Point out every malaria parasite.
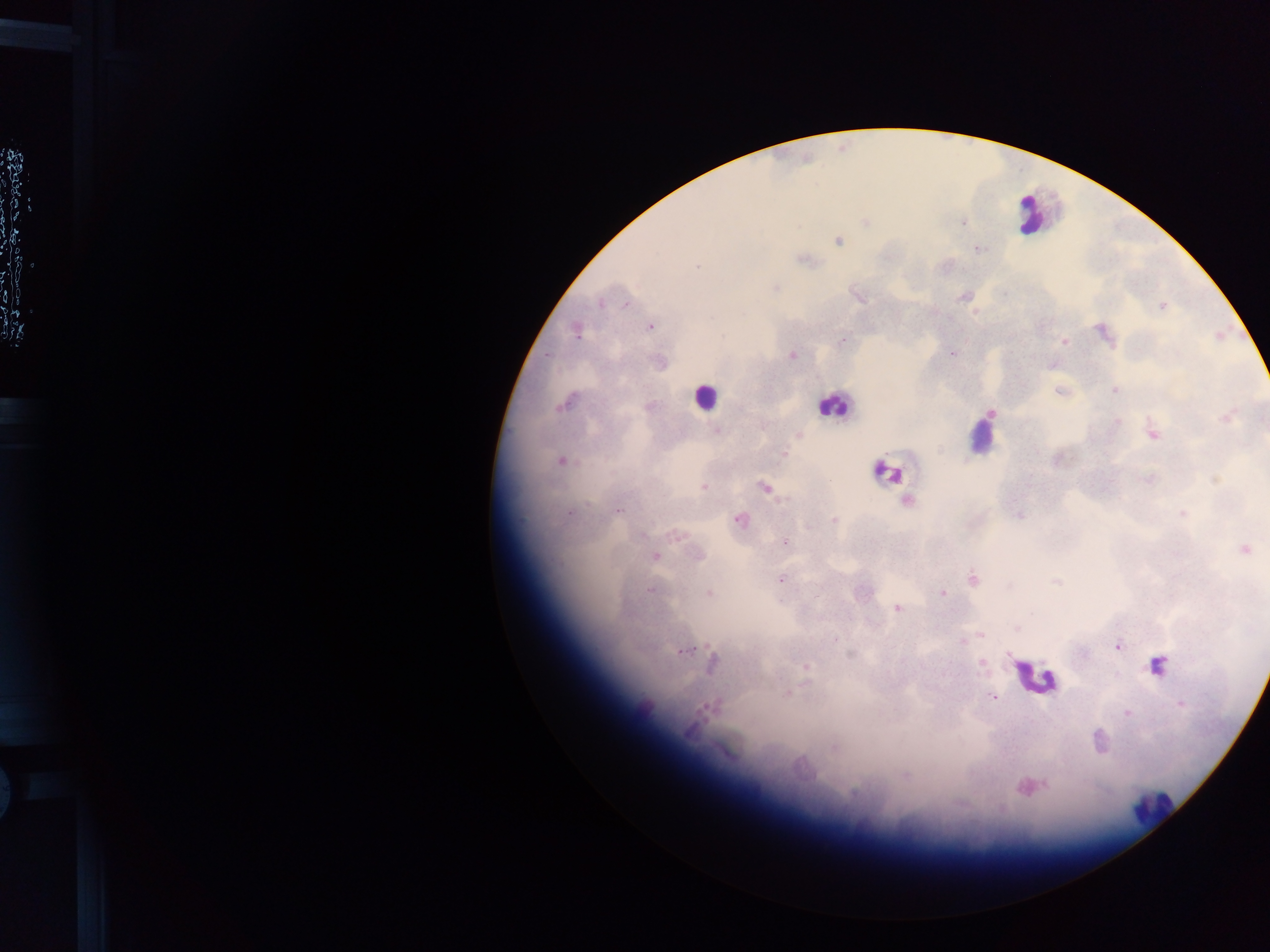
Approximate centers as (x, y) in pixels.
Malaria parasites: (964, 223), (839, 241), (981, 249), (808, 260), (775, 287), (963, 296), (859, 298), (601, 303), (624, 304), (1161, 307), (975, 313), (648, 327), (1099, 329), (574, 332), (722, 336), (843, 338), (1064, 342), (952, 353), (550, 355), (791, 355), (1112, 390), (1056, 391), (559, 405), (991, 413), (1151, 432), (798, 434), (784, 453), (560, 461), (764, 486), (703, 487), (906, 501), (569, 512), (1020, 517), (738, 519), (834, 519), (784, 543), (654, 556), (973, 579), (783, 580), (1056, 581), (1009, 586), (649, 590), (942, 593), (897, 610), (1018, 629), (835, 637), (1117, 645), (680, 653), (982, 665), (804, 666), (1156, 667), (785, 693), (993, 697), (1181, 705), (1128, 713), (1040, 789).

Summary:
  - Leukocyte locations: (1026, 216), (704, 399), (834, 403), (978, 440), (884, 471), (1038, 677), (1151, 807)
  - Country: Ghana
  - Image size: 1270×952 pixels
  - Field of view: single
  - Capture: mobile-phone photograph through a microscope
  - Preparation: thick blood film